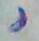
Toxoplasma gondii is shown. Micrograph. Captured at 1000x magnification.